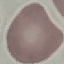
Summary:
  - Malaria status: uninfected
  - Image type: automatically extracted cell patch, resized to 64 × 64 pixels
  - Preparation: thin blood film
  - Capture: smartphone camera at the microscope eyepiece
  - Stain: Giemsa